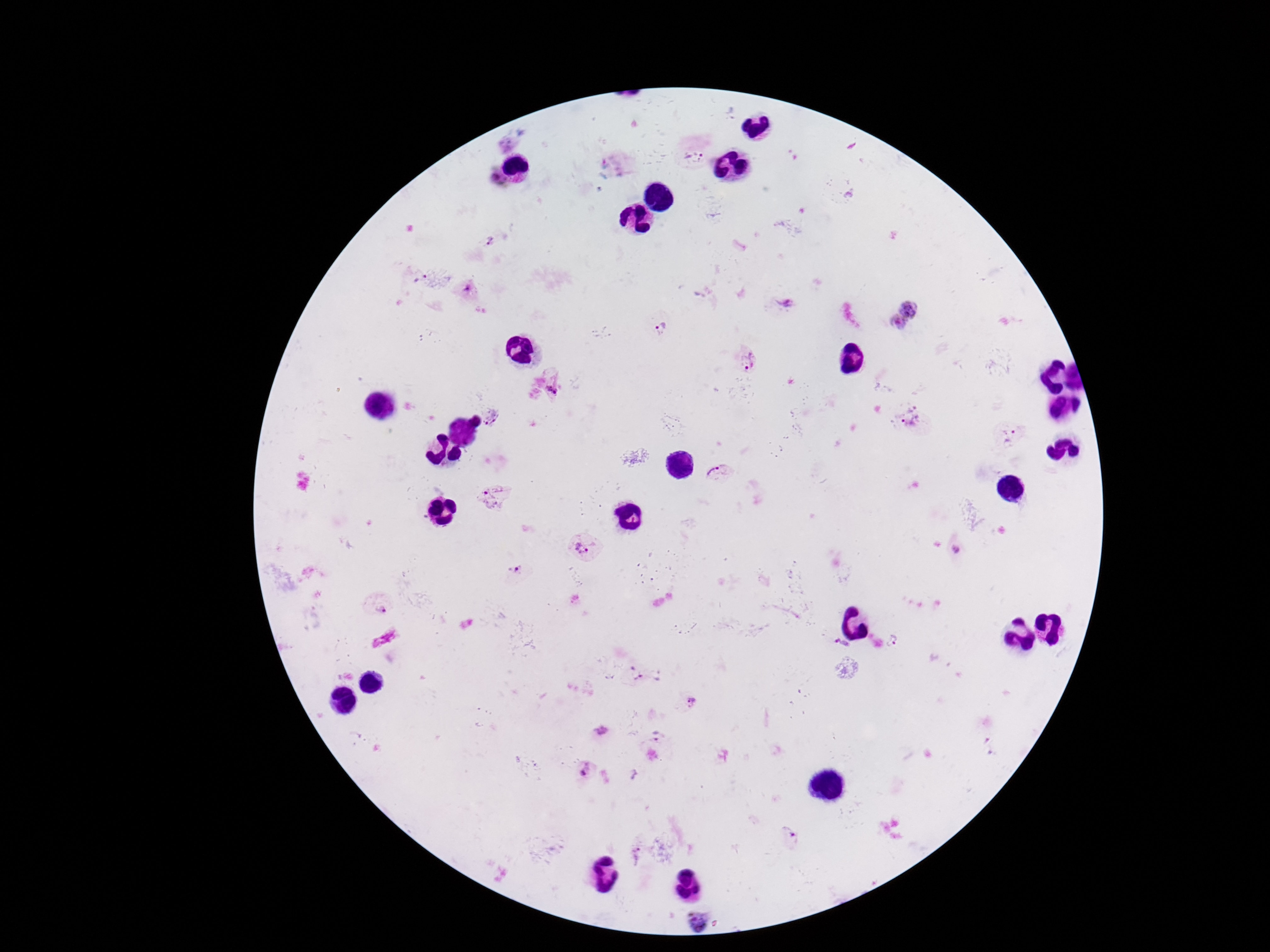
magnification = 100x
Plasmodium parasite locations = approximate centers as {x, y} in pixels: {695, 155}, {489, 241}, {423, 280}, {467, 288}, {782, 302}, {909, 308}, {897, 323}, {662, 328}, {748, 360}, {552, 390}, {491, 415}, {911, 423}, {1009, 438}, {717, 472}, {492, 498}, {583, 548}, {956, 549}, {517, 571}, {379, 602}, {893, 642}, {841, 646}, {634, 674}, {693, 701}, {601, 731}, {584, 768}, {788, 836}, {638, 855}, {699, 922}
stain = Giemsa
patient malaria status = positive
field of view = single
capture = smartphone camera through the microscope eyepiece
image size = 1270×952 pixels
preparation = thick peripheral-blood smear